Name the blood parasite species.
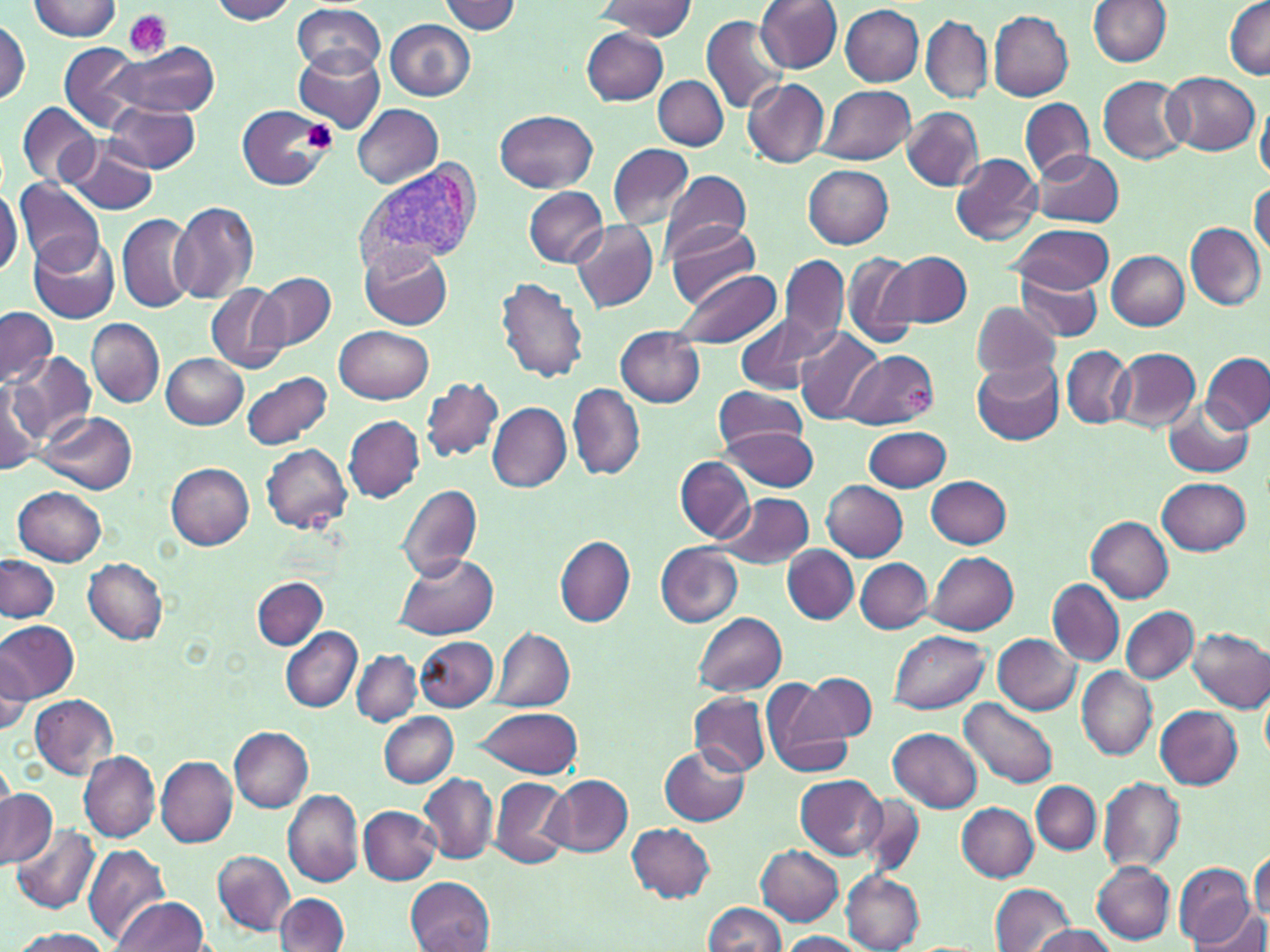

Plasmodium vivax.

magnification = 1000x
Plasmodium vivax-infected red blood cell locations = approximate bounding boxes as (x1,y1)-(x2,y2) corner pairs in pixels: (355,162)-(481,268)
platelet locations = approximate bounding boxes as (x1,y1)-(x2,y2) corner pairs in pixels: (123,10)-(170,58), (303,119)-(339,152), (903,386)-(933,414)
preparation = thin blood smear
uninfected red blood cell locations = approximate bounding boxes as (x1,y1)-(x2,y2) corner pairs in pixels: (209,0)-(297,24), (756,0)-(842,72), (1089,0)-(1171,66), (27,1)-(119,41), (437,1)-(521,34), (595,1)-(697,40), (1224,1)-(1269,78), (292,3)-(386,78), (839,3)-(924,86), (987,10)-(1073,101), (702,15)-(789,117), (922,15)-(991,103), (0,18)-(31,105), (385,18)-(477,101), (582,28)-(669,105), (109,40)-(220,118), (60,42)-(144,132), (294,49)-(387,129), (1164,72)-(1261,156), (1098,75)-(1191,164), (653,76)-(729,150), (742,77)-(830,168), (818,84)-(916,164), (1256,96)-(1270,184), (1020,98)-(1094,181), (108,100)-(200,173), (18,101)-(99,187), (236,104)-(333,191), (352,104)-(443,188), (902,106)-(984,191), (495,109)-(598,193), (62,136)-(159,214), (608,144)-(694,228), (1030,149)-(1124,226), (950,153)-(1042,245), (803,165)-(893,247), (659,169)-(752,260), (14,180)-(104,270), (1249,182)-(1269,256), (0,183)-(21,279), (523,186)-(608,267), (169,198)-(259,303), (117,213)-(195,314), (568,220)-(657,312), (662,221)-(760,307), (1008,222)-(1116,294), (1185,223)-(1266,310), (30,235)-(119,324), (362,245)-(452,329), (842,250)-(921,350), (1106,250)-(1190,330), (884,251)-(972,328), (781,254)-(847,347), (670,269)-(783,349), (1016,270)-(1103,340), (255,273)-(336,351), (496,276)-(589,383), (206,283)-(288,373), (972,301)-(1059,382), (0,307)-(57,388), (735,315)-(828,396), (87,318)-(164,407), (335,325)-(433,404), (794,327)-(886,422), (615,328)-(705,406), (1061,345)-(1134,428), (1111,347)-(1199,431), (839,350)-(939,428), (10,351)-(95,441), (1200,351)-(1270,434), (161,353)-(248,428), (972,358)-(1065,446), (241,372)-(333,450), (0,376)-(47,474), (421,376)-(503,463), (568,384)-(645,480), (714,387)-(808,450), (1164,401)-(1255,477), (487,402)-(570,492), (39,413)-(138,495), (344,415)-(424,501), (718,425)-(819,491), (864,425)-(950,492), (262,442)-(351,533), (675,457)-(753,544), (167,463)-(255,548), (926,475)-(1010,548), (1157,477)-(1251,553), (821,480)-(908,561), (397,483)-(482,581), (14,486)-(106,565), (714,491)-(815,569), (1087,516)-(1174,603), (556,536)-(635,626), (656,543)-(742,627), (783,546)-(860,623), (927,552)-(1018,635), (393,553)-(497,640), (1,555)-(59,623), (83,557)-(169,643), (855,558)-(932,634), (252,576)-(328,650), (1047,579)-(1124,666), (1121,607)-(1197,685), (694,612)-(787,697), (0,621)-(79,700), (281,628)-(361,712), (491,628)-(574,712), (1188,628)-(1270,712), (890,629)-(991,713), (993,633)-(1081,715), (415,636)-(499,710), (0,644)-(34,738), (351,650)-(420,726), (1076,667)-(1155,760), (800,673)-(876,742), (759,678)-(856,777), (690,693)-(769,776), (28,694)-(118,779), (962,698)-(1057,788), (477,704)-(583,778), (1154,705)-(1243,788), (379,713)-(458,786), (231,727)-(313,812), (888,727)-(982,812), (660,747)-(750,827), (79,751)-(161,844), (155,756)-(238,847), (419,772)-(497,863), (547,773)-(633,857), (795,775)-(888,860), (1100,776)-(1185,872), (490,777)-(571,869), (1031,782)-(1100,855), (0,789)-(56,869), (283,789)-(363,885), (860,792)-(926,877), (957,803)-(1037,881), (359,805)-(441,884), (627,823)-(716,904), (14,824)-(100,912), (756,843)-(844,926), (82,844)-(171,947), (212,850)-(295,936), (1249,850)-(1269,925), (1091,859)-(1175,943), (1173,862)-(1257,947), (841,872)-(924,951), (405,875)-(494,951), (991,882)-(1074,952), (274,892)-(350,951), (112,896)-(210,951), (703,902)-(786,951), (1197,910)-(1270,952), (1032,925)-(1114,952), (9,928)-(115,952), (777,931)-(867,951)
image size = 1270×952 pixels
modality = optical microscopy
stain = May-Grünwald-Giemsa
field of view = one of a larger specimen